Name the blood parasite species.
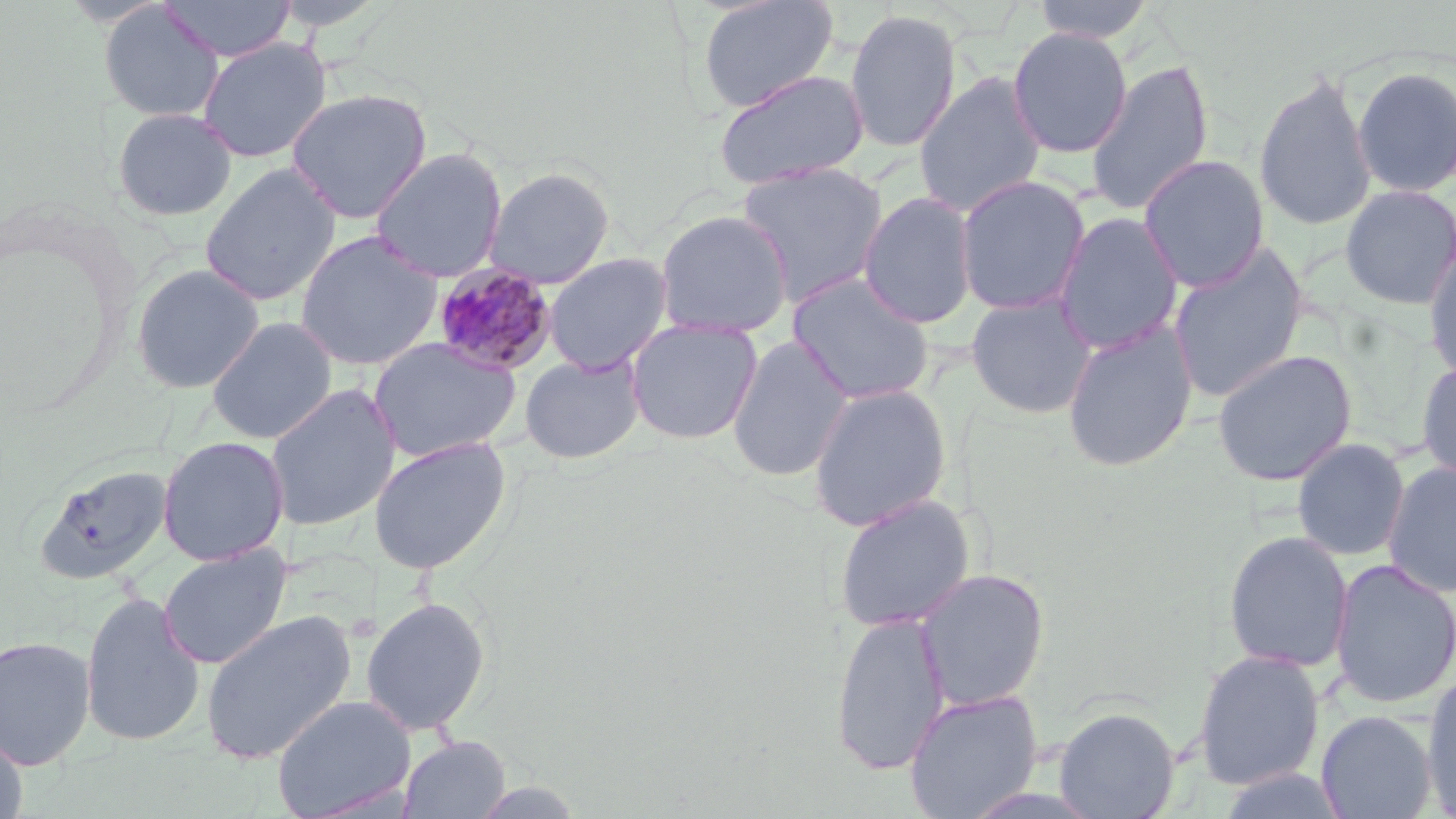

Plasmodium malariae.

Summary:
  - Coordinate format: approximate bounding boxes as (x1, y1, x2, y2) in pixels
  - Uninfected red blood cell locations: (158, 0, 295, 62), (697, 0, 838, 112), (1030, 0, 1157, 43), (98, 3, 224, 122), (844, 8, 962, 154), (1008, 27, 1132, 159), (197, 38, 330, 163), (1085, 58, 1215, 217), (1352, 65, 1456, 198), (712, 68, 870, 190), (1253, 71, 1376, 233), (914, 74, 1046, 217), (286, 89, 433, 224), (111, 107, 238, 221), (369, 147, 508, 283), (1139, 154, 1270, 292), (736, 162, 888, 307), (199, 163, 341, 307), (483, 167, 615, 289), (955, 175, 1090, 316), (1339, 184, 1456, 310), (858, 191, 978, 329), (654, 210, 794, 338), (1053, 211, 1183, 356), (295, 230, 443, 372), (1168, 242, 1310, 404), (1424, 243, 1456, 384), (543, 252, 672, 375), (129, 263, 265, 394), (787, 272, 935, 405), (965, 293, 1098, 419), (206, 316, 338, 444), (625, 317, 763, 445), (1061, 320, 1198, 473), (727, 335, 853, 483), (367, 336, 522, 463), (1212, 348, 1357, 486), (520, 353, 645, 464), (1416, 359, 1456, 487), (264, 383, 401, 532), (807, 383, 951, 532), (157, 435, 289, 565), (368, 436, 512, 575), (1293, 438, 1409, 560), (1382, 461, 1456, 598), (33, 462, 173, 585), (833, 493, 975, 633), (1222, 531, 1353, 673), (158, 543, 293, 670), (1329, 558, 1456, 710), (916, 568, 1050, 710), (79, 591, 206, 747), (361, 597, 490, 736), (199, 608, 357, 765), (830, 610, 949, 777), (0, 634, 97, 770), (1192, 648, 1325, 791), (1422, 671, 1456, 815), (904, 689, 1043, 819), (271, 694, 416, 819), (1053, 705, 1180, 819), (1316, 710, 1437, 819), (0, 727, 29, 819), (398, 735, 511, 819), (1214, 768, 1352, 819)
  - Plasmodium malariae-infected red blood cell locations: (431, 263, 559, 377)
  - Magnification: 1000x
  - Modality: light microscopy
  - Stain: May-Grünwald-Giemsa
  - Preparation: thin blood smear
  - Image size: 1456×819 pixels
  - Field of view: single